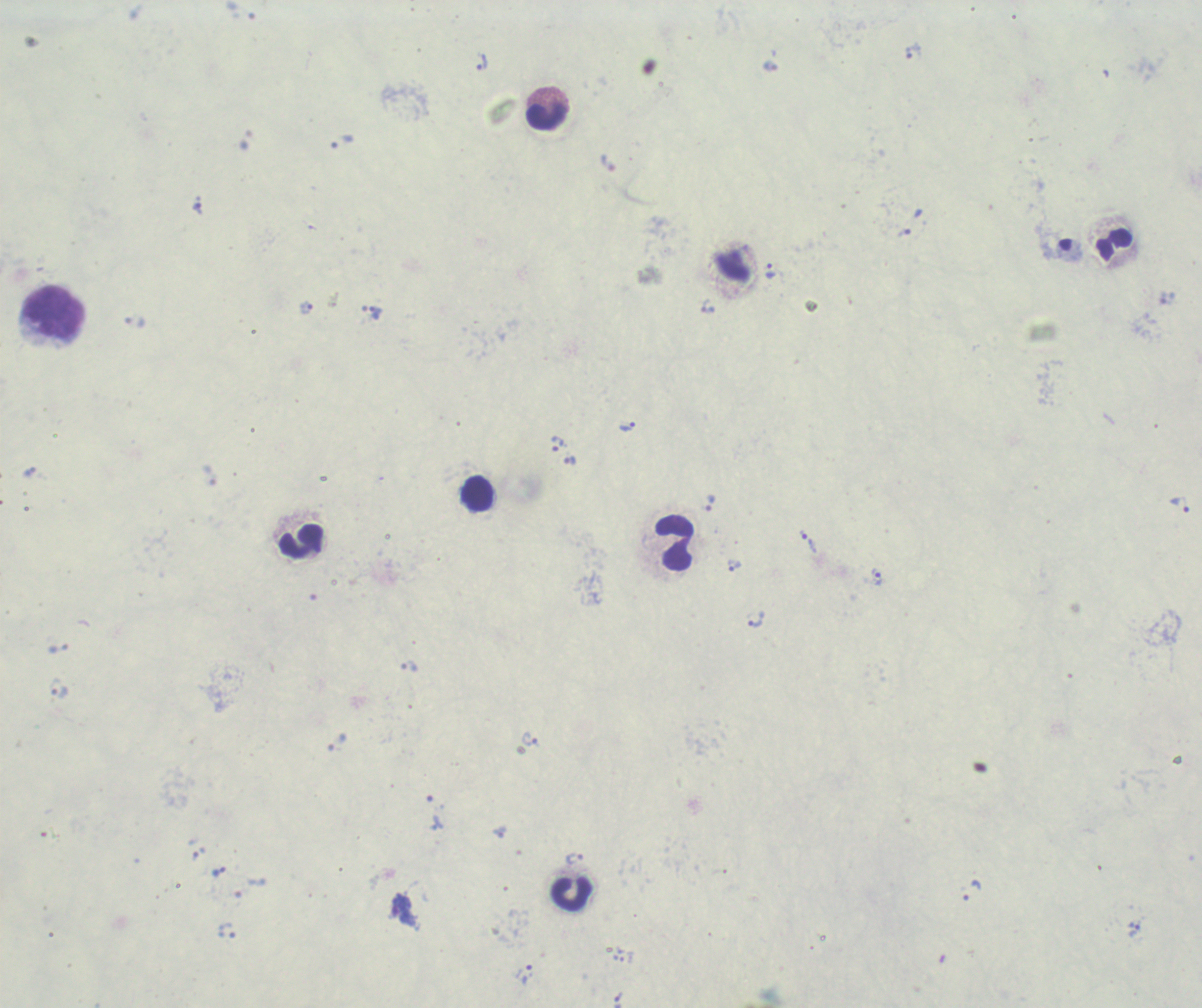 Approximate centers as [x, y] in pixels. Leukocyte locations: [547, 108], [1114, 245], [55, 312], [476, 493], [301, 540], [674, 543], [571, 894]. Trophozoite locations: [913, 51], [480, 62], [340, 141], [608, 163], [198, 209], [904, 233], [771, 270], [708, 306], [307, 308], [375, 312], [135, 322], [627, 426], [558, 443], [570, 461], [30, 471], [709, 502], [1180, 504], [809, 542], [733, 565], [877, 577], [757, 619], [410, 666], [59, 688], [531, 740], [337, 742], [500, 832], [574, 859], [218, 872], [972, 890], [1133, 930], [525, 974]. Background quality: poor. Thick blood smear. Previously used in a real diagnosis. 100x magnification. Image is 1202×1008 pixels. Romanowsky stain. Result: positive for Plasmodium parasites. Single field of view.